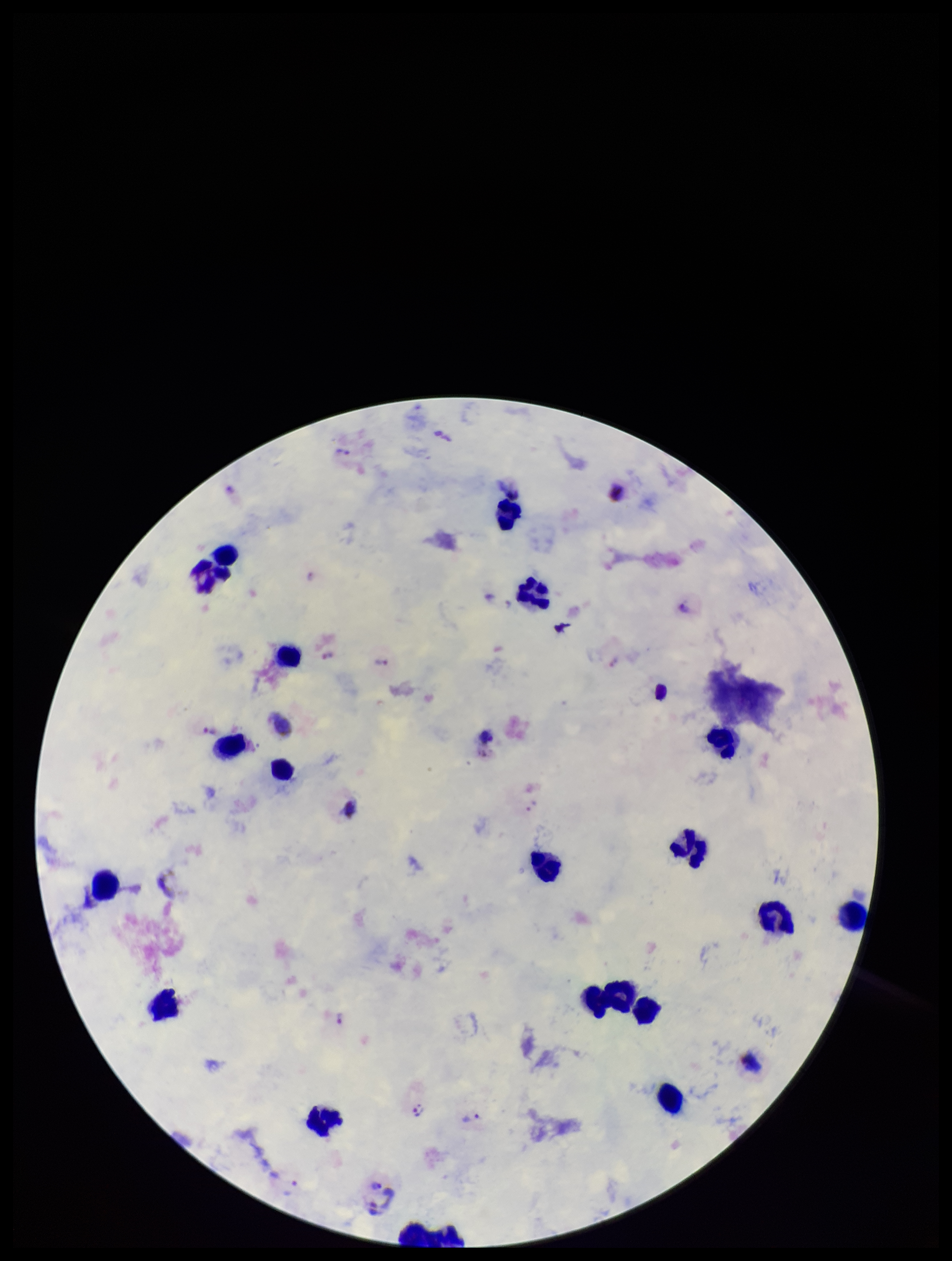

Summary:
  - Capture: smartphone photograph through the microscope eyepiece
  - Field of view: one from this slide
  - Image size: 952×1261 pixels
  - Stain: Giemsa
  - Patient malaria status: infected
  - Parasite count: 8
  - Species reported for this patient: Plasmodium vivax
  - Plasmodium parasites: identified
  - Preparation: thick
  - Leukocyte count: 20